Classify this cell by malaria status.
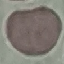
Uninfected.

Giemsa-stained preparation. Thin smear of blood. Automatically extracted cell patch, resized to 64 × 64 pixels. Acquired by smartphone through the microscope eyepiece.